Classify this cell by malaria status.
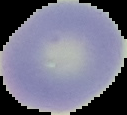
It is uninfected.

preparation = thin blood smear
image size = 127×115 pixels
image type = segmented cell region with the area outside set to black